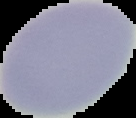

Summary:
  - Preparation: thin blood smear
  - Image type: cell region segmented out of the field of view; surrounding area masked to black
  - Malaria status: uninfected
  - Image size: 136×118 pixels